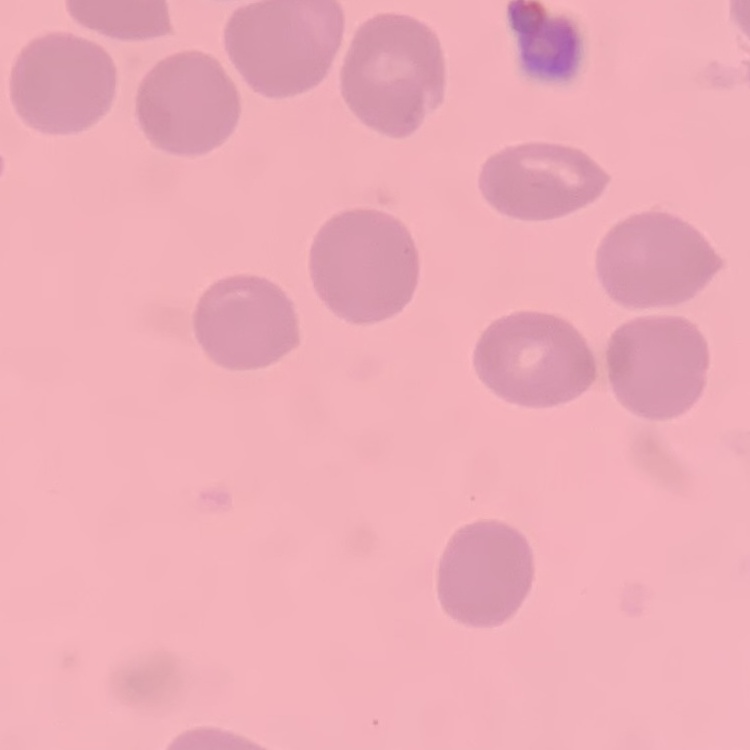

The erythrocytes show no rouleaux formation. Thin blood smear. One tile cut from a larger photomicrograph. Stained with either Field's or Giemsa.